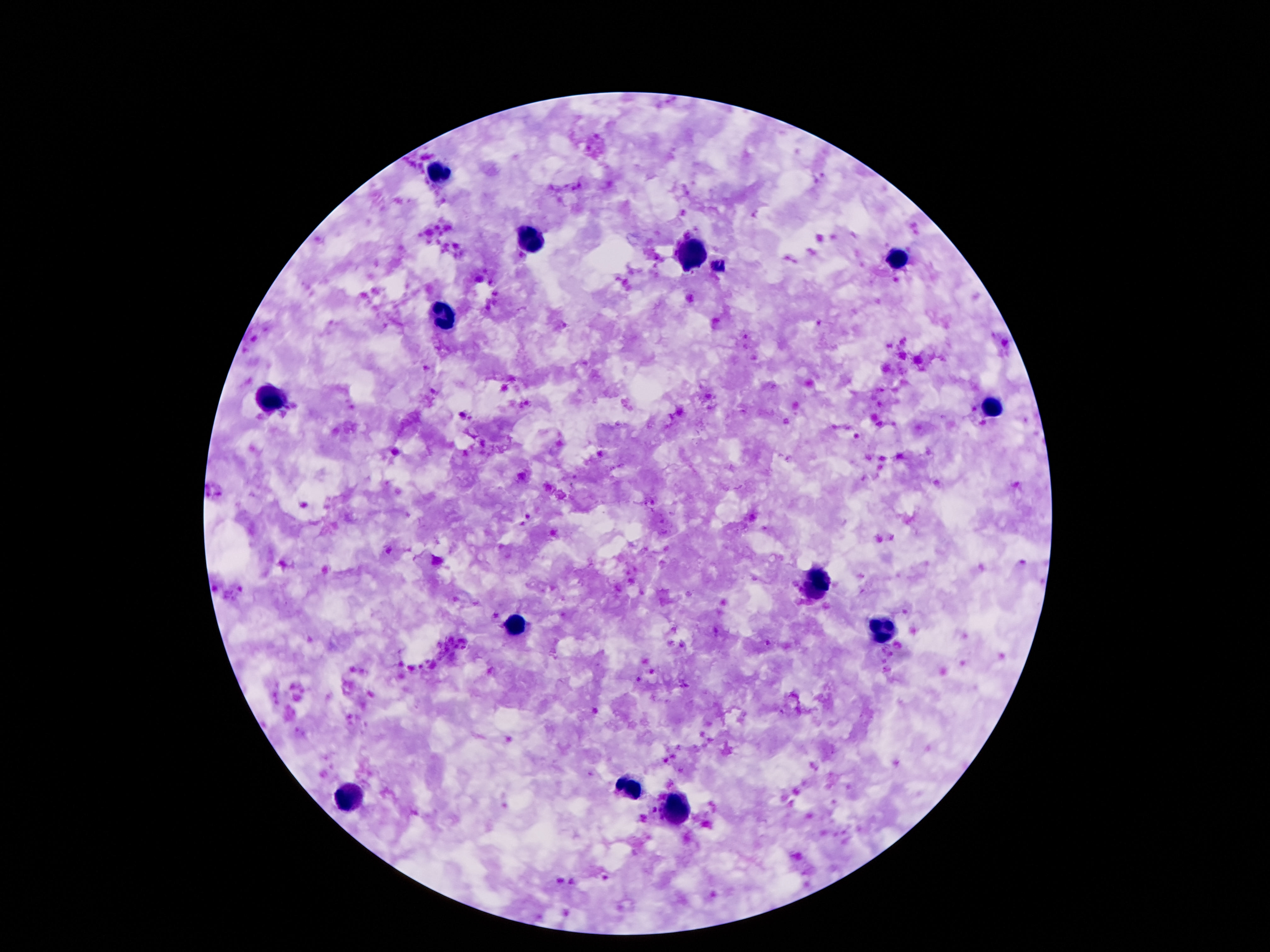
stain = Giemsa
field of view = single
leukocyte locations = approximate centers as {x, y} in pixels: {439, 176}, {533, 241}, {693, 256}, {903, 258}, {441, 315}, {267, 399}, {989, 408}, {817, 584}, {515, 626}, {628, 785}, {351, 796}, {678, 813}
image size = 1270×952 pixels
preparation = thick blood film
magnification = 100x
patient malaria status = uninfected
capture = smartphone camera through the microscope eyepiece